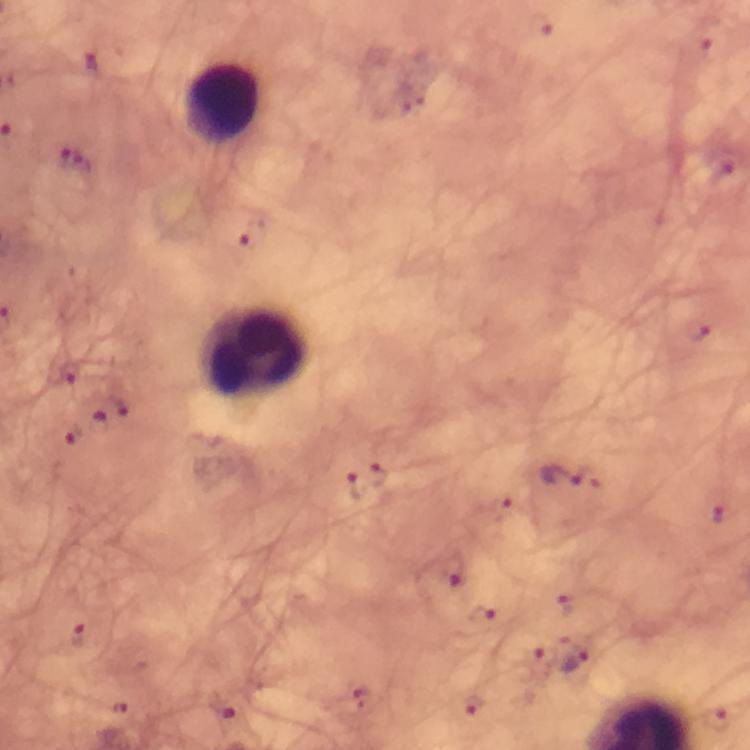

leukocyte locations = approximate centers as [x, y] in pixels: [220, 105], [256, 349]
malaria parasite locations = approximate centers as [x, y] in pixels: [94, 61], [77, 159], [254, 233], [68, 372], [120, 406], [99, 415], [75, 434], [377, 475], [562, 476], [355, 485], [576, 658]
image size = 750×750 pixels
stain = Giemsa
magnification = 100x
immersion oil = used
cropped from = a single field of view
context = from a diagnostic examination for malaria
capture = smartphone photograph through a microscope
preparation = thick smear